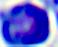

Summary:
  - Modality: photomicrograph
  - Magnification: 400x
  - Identification: white blood cell